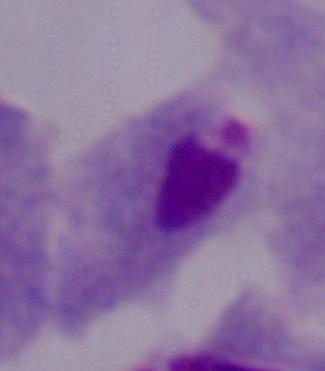
magnification = 1000x
identification = trichomonad
modality = photomicrograph